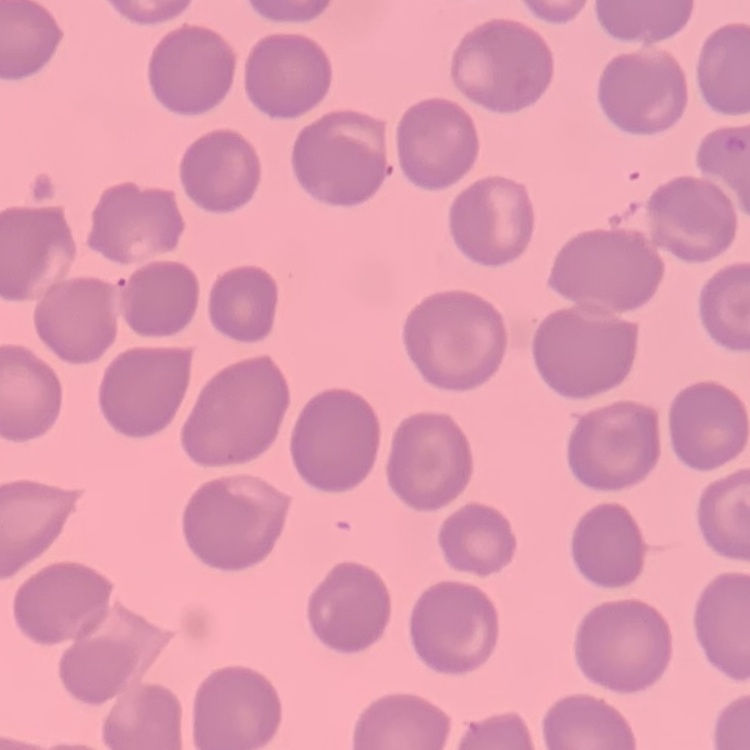

erythrocyte morphology = no rouleaux formation
image type = square crop of a larger photomicrograph
stain = Field's or Giemsa
preparation = thin blood film